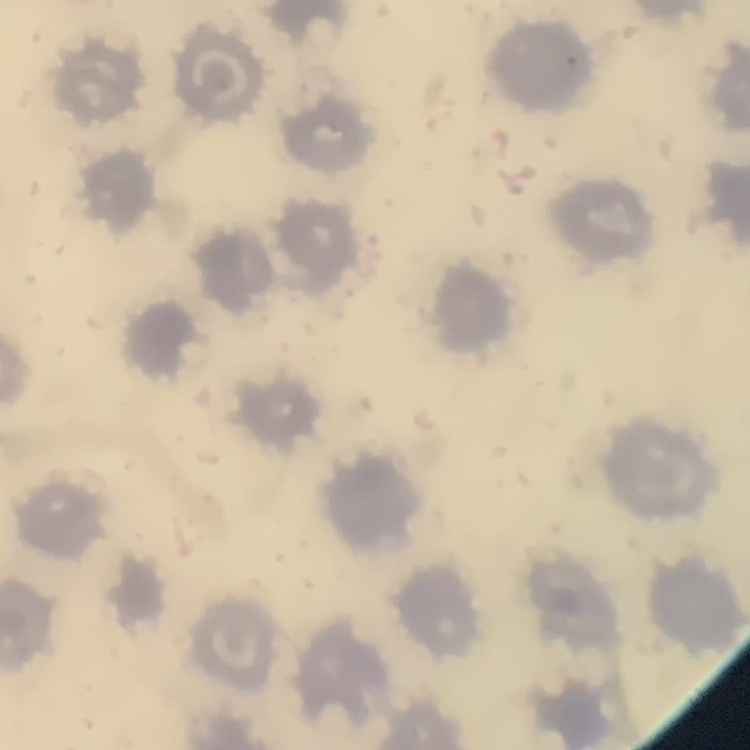

Summary:
  - Red blood cell morphology: no rouleaux formation
  - Stain: Field's or Giemsa
  - Image type: square crop of a larger photomicrograph
  - Preparation: thin blood smear